Assess this cell for malaria.
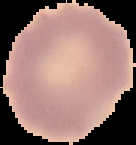

It is uninfected.

preparation: thin blood smear
image_type: segmented cell region on a black background
image_size: 136×145 pixels